Locate every Plasmodium parasite.
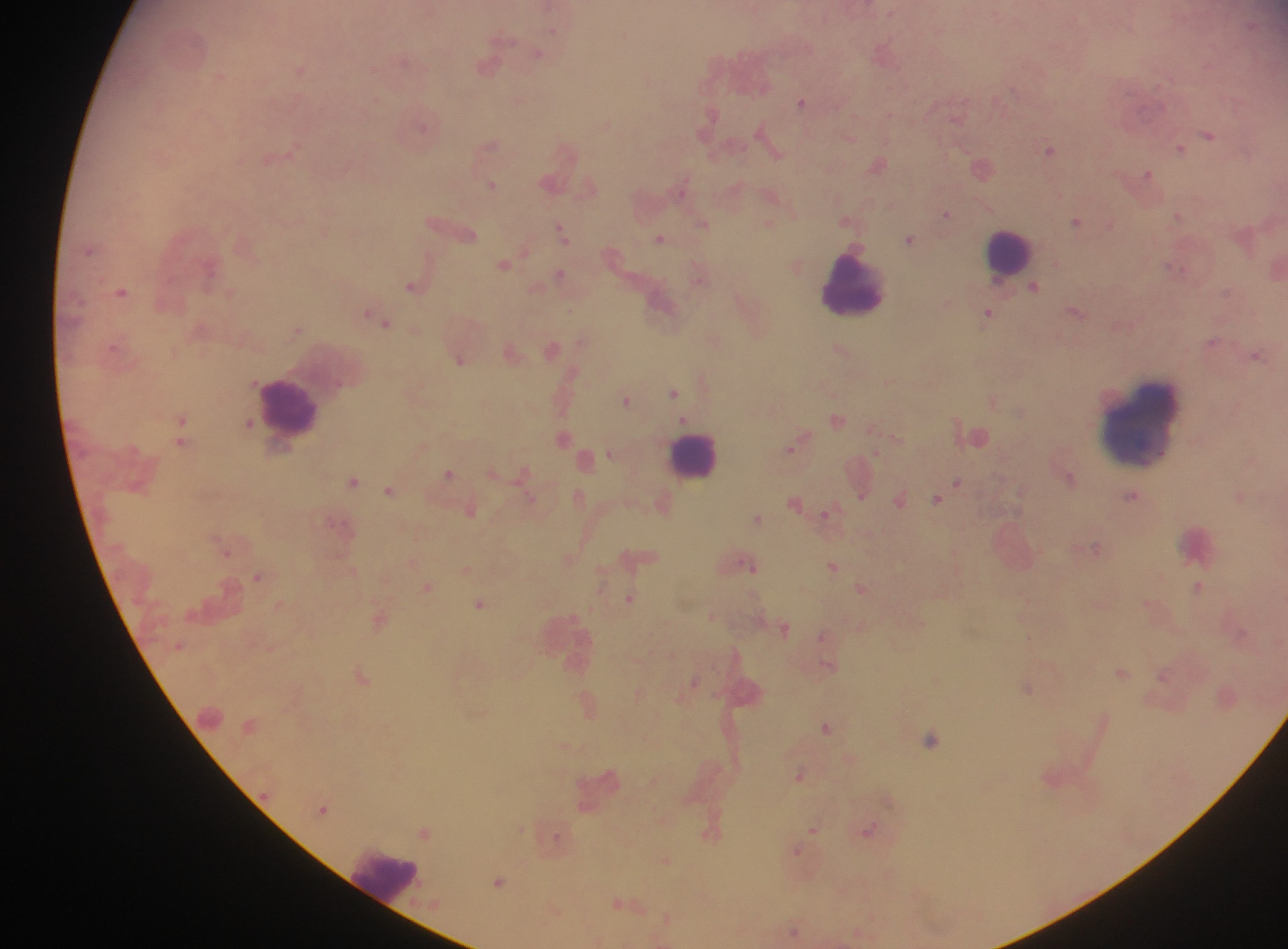

Approximate centers as (x, y) in pixels.
Plasmodium parasites: (538, 53), (884, 53), (406, 59), (487, 64), (300, 67), (220, 76), (520, 99), (802, 101), (957, 114), (708, 118), (425, 125), (1210, 133), (767, 137), (489, 146), (1051, 148), (1181, 148), (568, 151), (278, 155), (879, 164), (982, 166), (1147, 175), (551, 182), (492, 184), (681, 188), (947, 214), (1179, 216), (849, 220), (1077, 220), (704, 223), (450, 226), (563, 231), (660, 238), (910, 239), (505, 263), (796, 264), (1276, 268), (560, 275), (700, 276), (415, 285), (1035, 286), (122, 291), (663, 303), (1077, 311), (988, 314), (380, 319), (297, 328), (583, 341), (1213, 341), (552, 348), (842, 350), (511, 352), (1256, 355), (459, 357), (704, 382), (674, 392), (626, 399), (993, 400), (837, 419), (182, 423), (249, 423), (974, 433), (182, 435), (565, 437), (897, 437), (571, 441), (797, 443), (611, 452), (586, 459), (493, 471), (523, 473), (449, 474), (1070, 477), (353, 480), (861, 482), (958, 483), (391, 490), (579, 496), (861, 496), (1131, 496), (1240, 496), (900, 498), (937, 498), (530, 499), (796, 501), (663, 503), (471, 509), (829, 514), (758, 518), (1097, 548), (226, 549), (639, 556), (569, 557), (747, 563), (833, 566), (467, 569), (258, 575), (603, 583), (1199, 586), (428, 587), (862, 587), (630, 597), (480, 603), (1150, 603), (713, 615), (380, 619), (784, 627), (827, 638), (1122, 672), (1165, 674), (362, 675), (695, 680), (1028, 687), (639, 694), (1228, 695), (589, 704), (1104, 722), (827, 726), (930, 739), (565, 745), (801, 775), (324, 808), (814, 829), (868, 830), (424, 831), (712, 832), (558, 838), (798, 851), (666, 860), (499, 881), (626, 906), (555, 911), (667, 919), (796, 931), (861, 934).

capture = mobile-phone photograph through a microscope
leukocyte locations = approximate centers as (x, y) in pixels: (1008, 254), (851, 283), (290, 408), (1144, 423), (693, 455), (1198, 543), (566, 639), (210, 718), (384, 875)
field of view = single
image size = 1288×949 pixels
country = Ghana
preparation = thick blood smear